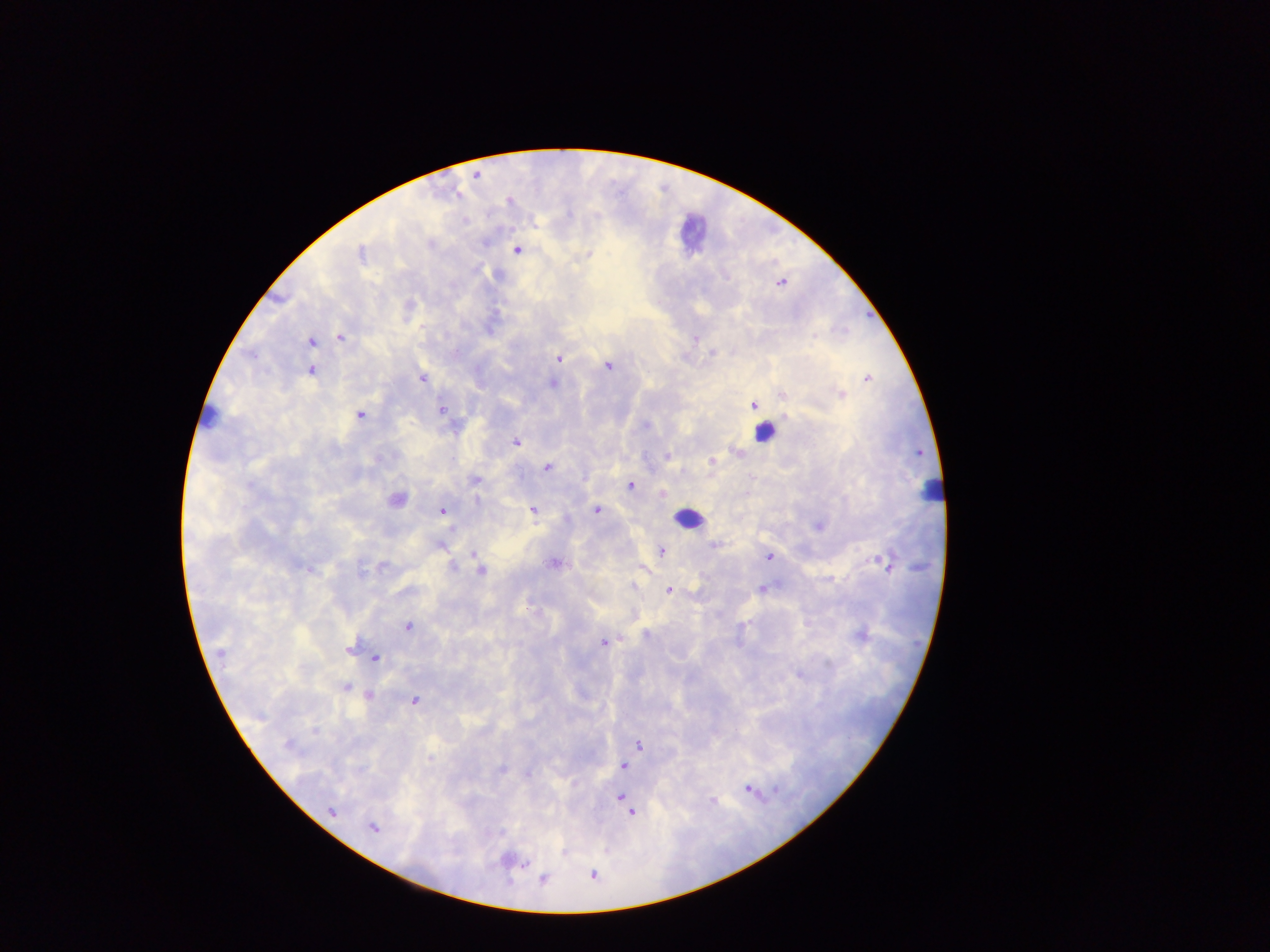
Approximate centers as [x, y] in pixels.
Summary:
  - Plasmodium parasite locations: [476, 175], [465, 221], [431, 245], [518, 250], [360, 253], [589, 254], [781, 283], [488, 331], [814, 335], [340, 337], [696, 339], [310, 342], [712, 352], [558, 358], [607, 366], [311, 370], [867, 378], [422, 379], [553, 383], [842, 394], [784, 395], [753, 405], [441, 410], [361, 415], [516, 443], [737, 452], [667, 456], [711, 460], [546, 467], [475, 480], [630, 485], [663, 492], [396, 499], [477, 500], [442, 510], [532, 510], [596, 510], [819, 526], [440, 544], [713, 545], [662, 551], [473, 553], [768, 557], [885, 563], [555, 564], [382, 565], [452, 566], [481, 570], [633, 586], [763, 588], [669, 589], [408, 627], [647, 634], [860, 635], [603, 643], [348, 650], [221, 652], [376, 658], [345, 687], [368, 696], [415, 700], [314, 730], [289, 746], [639, 746], [623, 766], [502, 769], [528, 775], [748, 788], [775, 789], [620, 797], [713, 801], [627, 807], [332, 811], [631, 813], [372, 827], [524, 864], [593, 875], [543, 879]
  - Leukocyte locations: [689, 232], [763, 432], [931, 492], [689, 519]
  - Country: Ghana
  - Image size: 1270×952 pixels
  - Capture: mobile-phone photograph through a microscope
  - Preparation: thick blood smear
  - Field of view: single